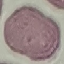

Malaria status: uninfected. Cell patch, automatically extracted from a larger field of view and resized to 64 × 64 pixels. Photographed with a smartphone camera at the microscope eyepiece. Thin smear of blood. Giemsa-stained preparation.